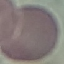
malaria status = uninfected
preparation = thin smear
capture = smartphone camera at the microscope eyepiece
stain = Giemsa
image type = automatically extracted cell patch, resized to 64 × 64 pixels